Report the malaria status of this cell.
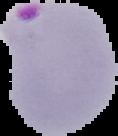
It is parasitized.

From a thin blood smear. Cell region segmented out of the field of view; the surrounding area is masked to black. Image is 118×136 pixels.